Report the malaria status of this cell.
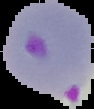
It is parasitized.

{
  "preparation": "thin blood film",
  "image_size": "94×109 pixels",
  "image_type": "segmented cell region on a black background"
}